Assess the morphology of the red blood cells.
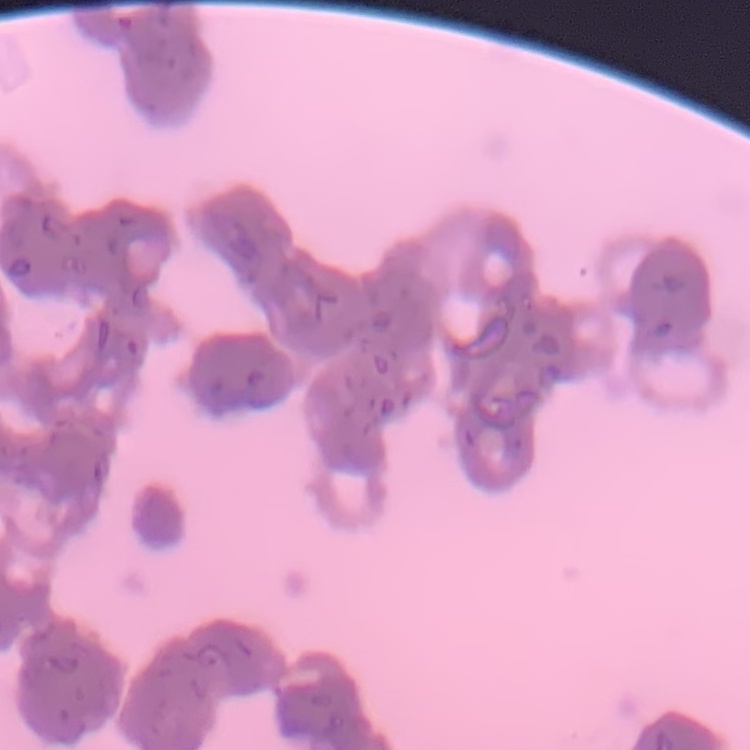

They show rouleaux formation.

image type = one tile cut from a larger photomicrograph
preparation = thin blood smear
stain = Field's or Giemsa